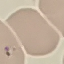

Summary:
  - Malaria status: parasitized
  - Image type: automatically extracted cell patch, resized to 64 × 64 pixels
  - Preparation: thin blood film
  - Stain: Giemsa
  - Capture: smartphone through the microscope eyepiece